Assess this cell for malaria.
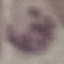

Uninfected.

Thin blood smear. Photographed with a smartphone camera at the microscope eyepiece. Cell patch, automatically extracted from a larger field of view and resized to 64 × 64 pixels. Giemsa stain.